Name the parasite shown.
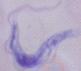
A trypanosome.

Micrograph. 1000x magnification.